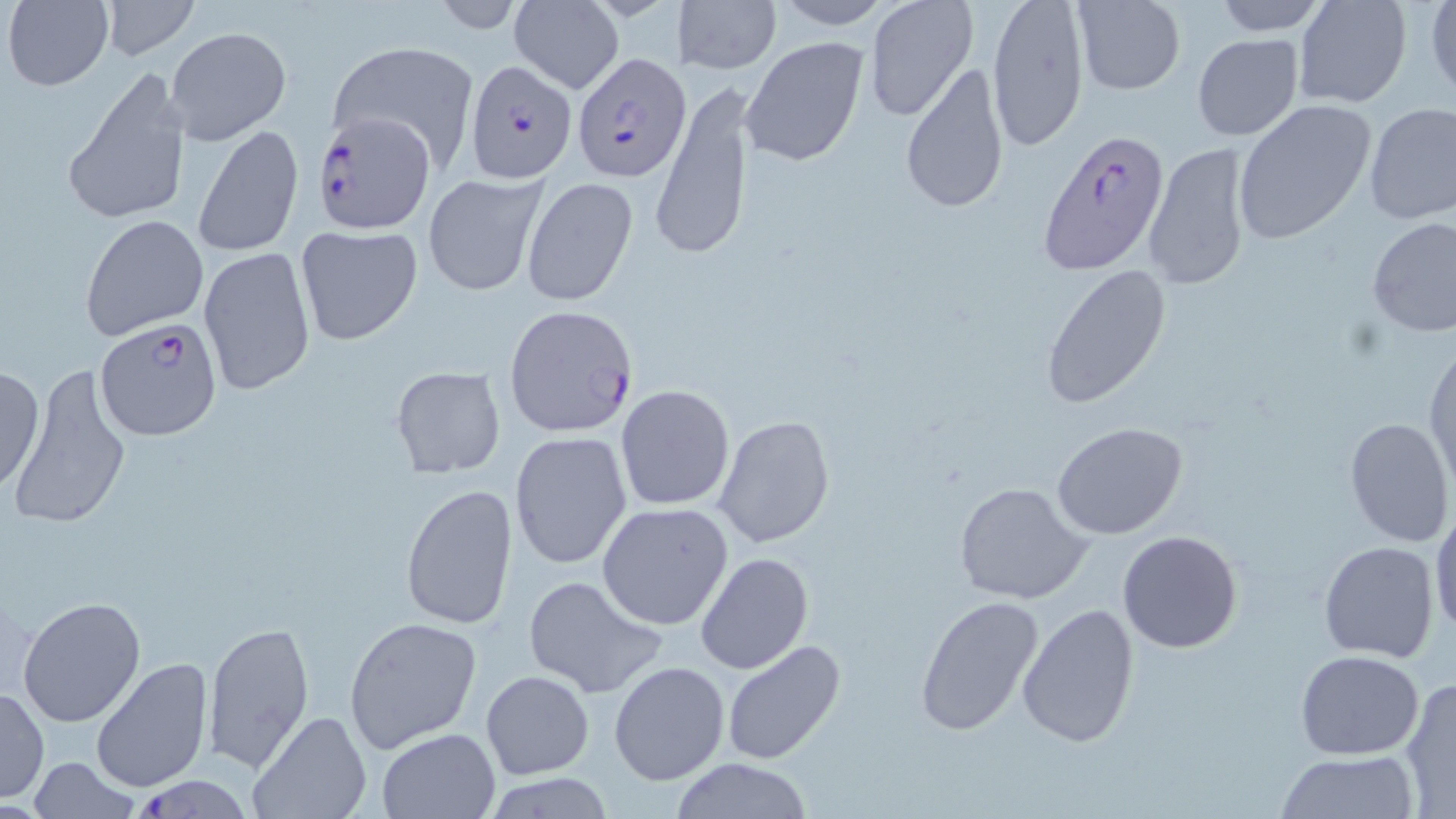

slide-level diagnosis = Plasmodium falciparum
preparation = thin blood smear
uninfected red blood cell locations = approximate bounding boxes as (x1,y1)-(x2,y2) corner pairs in pixels: (4,0)-(113,91), (671,0)-(781,76), (864,0)-(979,122), (986,0)-(1090,152), (1294,0)-(1412,108), (1425,0)-(1456,99), (508,1)-(623,93), (770,1)-(898,30), (1211,1)-(1334,35), (99,2)-(195,60), (1069,2)-(1185,98), (169,26)-(292,144), (1192,33)-(1304,140), (740,35)-(871,169), (327,40)-(479,172), (899,61)-(1010,216), (63,68)-(190,228), (653,79)-(756,261), (1231,100)-(1376,246), (1363,103)-(1456,225), (193,123)-(303,257), (1141,141)-(1254,292), (421,170)-(547,297), (520,176)-(639,306), (81,213)-(206,341), (1366,215)-(1456,338), (295,225)-(424,346), (198,246)-(316,395), (1040,263)-(1173,408), (1425,337)-(1456,496), (0,362)-(45,495), (391,363)-(508,477), (6,367)-(134,532), (616,384)-(734,510), (713,413)-(836,550), (1343,417)-(1454,547), (1051,420)-(1188,539), (510,433)-(633,568), (954,481)-(1095,606), (401,483)-(518,630), (597,502)-(734,631), (1431,505)-(1455,643), (1117,530)-(1243,653), (1319,541)-(1440,664), (696,552)-(814,675), (521,574)-(667,699), (18,595)-(147,727), (914,595)-(1044,738), (1018,601)-(1141,748), (343,616)-(481,754), (201,620)-(314,770), (721,638)-(847,765), (1296,649)-(1424,760), (90,657)-(214,795), (608,660)-(729,786), (481,670)-(594,778), (1398,677)-(1456,816), (0,687)-(48,803), (249,711)-(369,819), (376,728)-(500,818), (1274,750)-(1420,818), (27,758)-(142,818), (667,758)-(818,817)
magnification = 1000x
image size = 1456×819 pixels
field of view = single
stain = May-Grünwald-Giemsa
modality = optical microscopy
Plasmodium falciparum-infected red blood cell locations = approximate bounding boxes as (x1,y1)-(x2,y2) corner pairs in pixels: (570,52)-(692,180), (464,57)-(577,180), (313,112)-(442,237), (1036,128)-(1169,277), (505,306)-(640,436), (94,318)-(222,440), (133,775)-(254,816)